Classify this cell by malaria status.
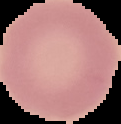
It is uninfected.

The area outside the segmented cell region is set to black. From a thin blood smear. Image is 121×124 pixels.